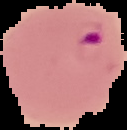

Summary:
  - Image type: cell region segmented out of the field of view; surrounding area masked to black
  - Result: malaria parasites detected
  - Image size: 127×130 pixels
  - Preparation: thin blood film